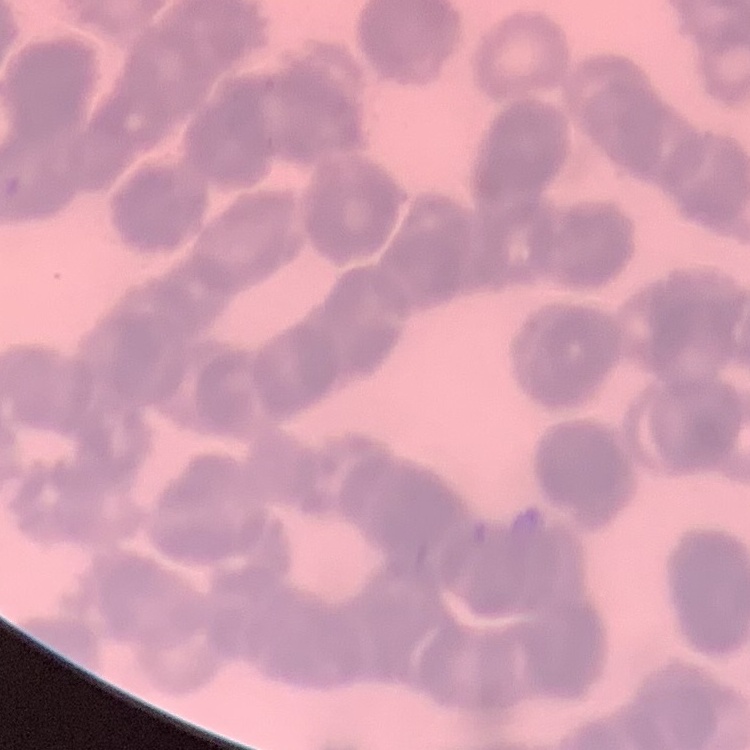 The erythrocytes show rouleaux formation. Thin blood smear. Field's or Giemsa stain. One tile cut from a larger photomicrograph.